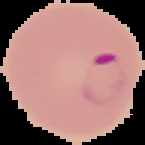
Summary:
  - Image type: segmented cell region on a black background
  - Image size: 145×145 pixels
  - Result: malaria parasites identified
  - Preparation: thin blood film